Outline each uninfected red blood cell.
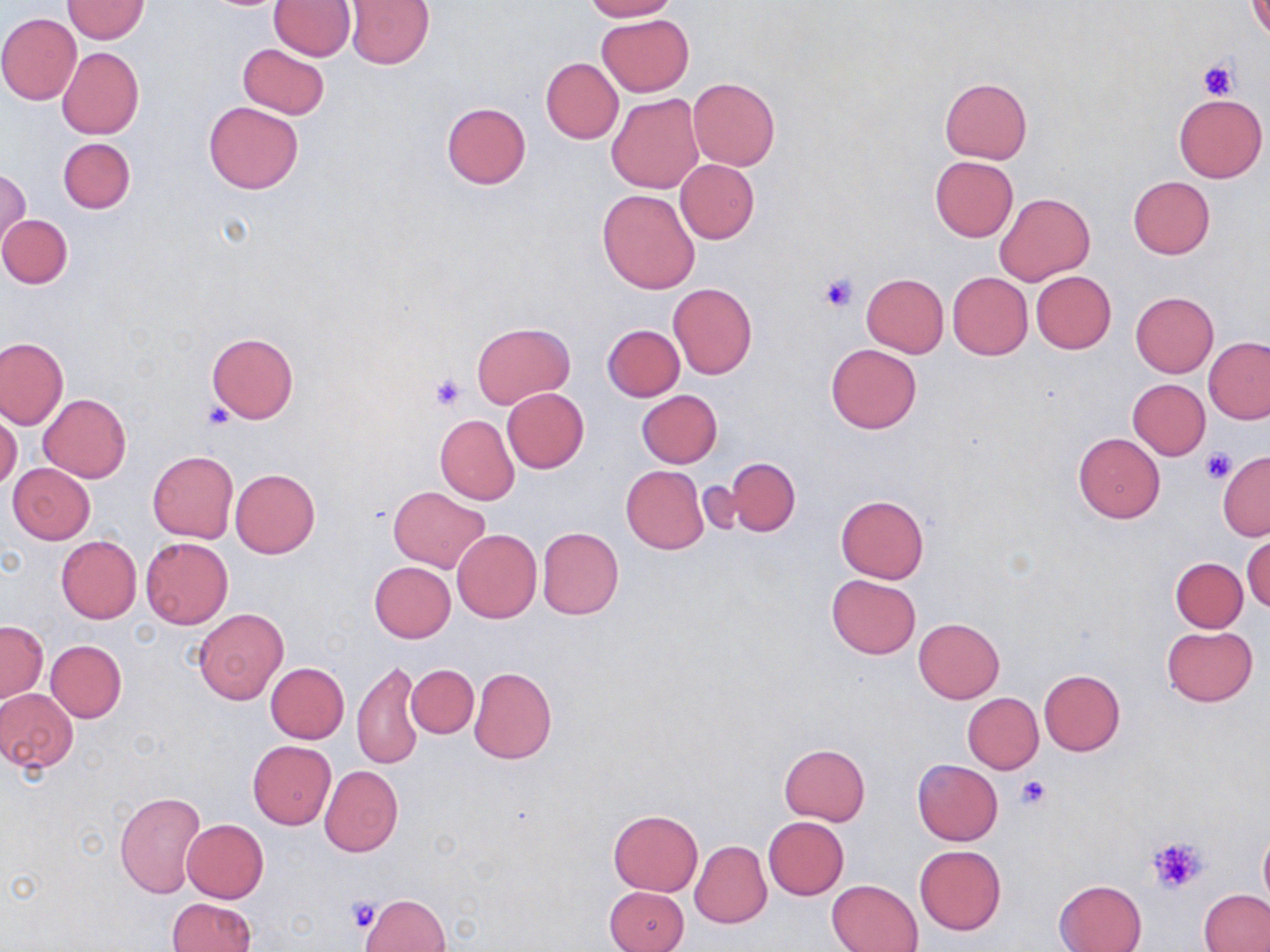

Approximate bounding boxes as (x1, y1, x2, y2) in pixels.
Uninfected red blood cells: (63, 0, 149, 43), (269, 0, 355, 59), (581, 0, 677, 21), (1249, 0, 1270, 40), (344, 1, 435, 68), (596, 13, 693, 96), (0, 14, 81, 104), (238, 43, 329, 119), (57, 47, 144, 139), (541, 57, 623, 143), (688, 77, 780, 169), (940, 78, 1033, 163), (608, 93, 704, 194), (1173, 93, 1267, 183), (203, 101, 303, 194), (441, 101, 531, 188), (58, 137, 134, 214), (930, 155, 1018, 242), (675, 159, 759, 244), (1, 168, 30, 248), (1127, 177, 1215, 260), (598, 189, 700, 293), (995, 193, 1094, 284), (0, 214, 73, 288), (1031, 271, 1116, 354), (947, 272, 1032, 359), (862, 274, 949, 357), (668, 282, 757, 378), (1131, 291, 1218, 376), (473, 322, 574, 408), (602, 324, 684, 401), (206, 333, 298, 422), (0, 336, 68, 430), (1204, 336, 1270, 423), (826, 343, 922, 434), (1128, 379, 1210, 459), (502, 387, 589, 473), (637, 389, 723, 468), (39, 394, 131, 483), (0, 411, 22, 490), (435, 415, 519, 504), (1073, 433, 1165, 522), (147, 451, 238, 542), (1218, 451, 1270, 540), (724, 458, 800, 536), (9, 464, 94, 543), (621, 465, 709, 555), (230, 468, 320, 558), (388, 487, 489, 573), (836, 494, 929, 583), (537, 527, 624, 620), (452, 529, 541, 622), (1243, 533, 1270, 614), (56, 535, 142, 624), (140, 537, 233, 628), (1170, 557, 1248, 632), (369, 561, 456, 642), (827, 574, 921, 659), (193, 608, 288, 704), (914, 618, 1004, 702), (0, 621, 48, 700), (1163, 626, 1257, 706), (46, 640, 126, 722), (352, 659, 423, 770), (265, 662, 349, 743), (406, 665, 478, 738), (469, 667, 556, 764), (1039, 669, 1125, 754), (0, 688, 78, 773), (963, 693, 1043, 772), (247, 741, 335, 828), (779, 744, 870, 825), (911, 759, 1002, 845), (320, 766, 403, 856), (114, 791, 207, 897), (608, 810, 702, 895), (764, 817, 849, 899), (182, 819, 268, 903), (1258, 825, 1270, 914), (690, 841, 771, 929), (914, 845, 1006, 934), (828, 879, 923, 952), (1054, 879, 1147, 952), (605, 886, 689, 952), (1200, 890, 1270, 951), (360, 893, 449, 952), (167, 898, 256, 952).

slide-level diagnosis = no evidence of blood parasites
platelet locations = approximate bounding boxes as (x1, y1, x2, y2) in pixels: (1198, 59, 1239, 99), (817, 271, 861, 313), (429, 373, 467, 409), (202, 403, 234, 429), (1199, 448, 1237, 484), (1015, 775, 1051, 810), (1147, 836, 1208, 894), (345, 897, 382, 932)
stain = May-Grünwald-Giemsa
field of view = one of a larger specimen
magnification = 1000x
image size = 1270×952 pixels
modality = light microscopy
preparation = thin blood film